Report the malaria status of this cell.
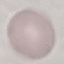

Uninfected.

Summary:
  - Stain: Giemsa
  - Capture: smartphone camera at the microscope eyepiece
  - Preparation: thin blood film
  - Image type: automatically extracted cell patch, resized to 64 × 64 pixels